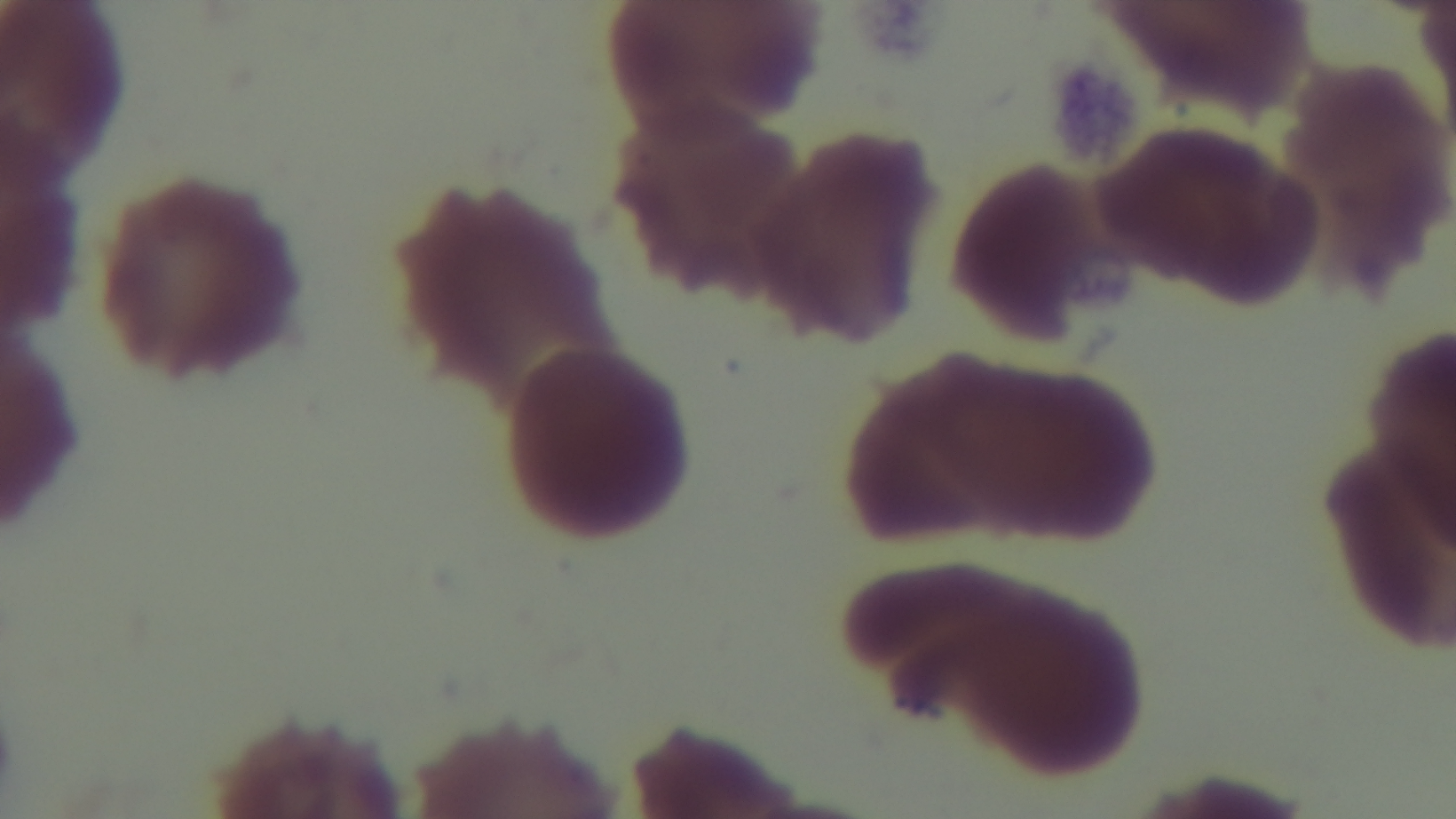

Summary:
  - Field of view: one from the slide
  - Malaria status: negative
  - Objective: 100x oil immersion
  - Preparation: thin smear
  - Stain: Giemsa
  - Modality: light microscopy
  - Capture: mounted 4K digital camera